Identify the cell.
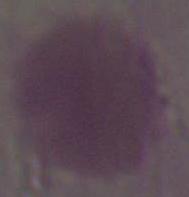
An erythrocyte.

modality = micrograph
magnification = 1000x